Comment on the morphology of the red blood cells.
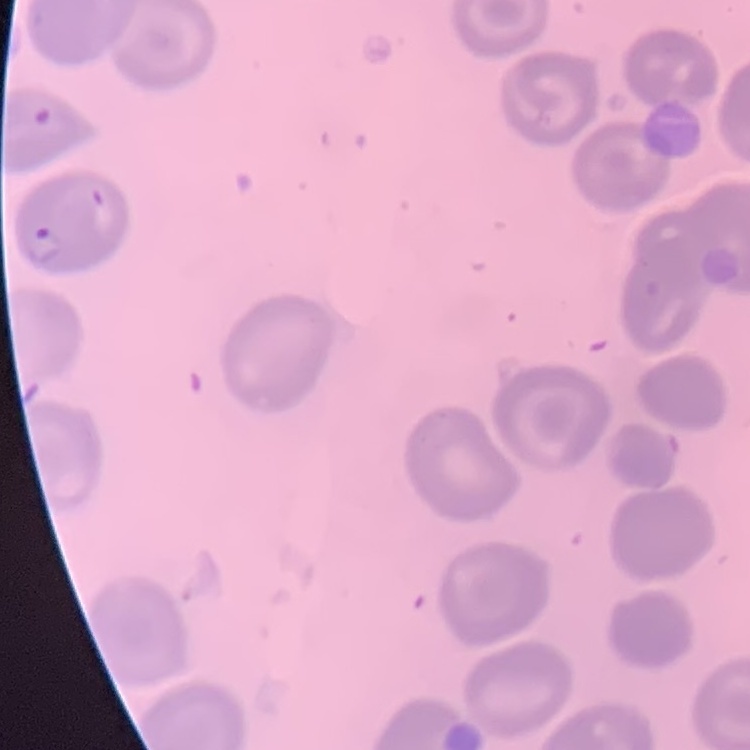

They show no rouleaux formation.

Summary:
  - Image type: square crop of a larger photomicrograph
  - Preparation: thin peripheral smear
  - Stain: Field's or Giemsa